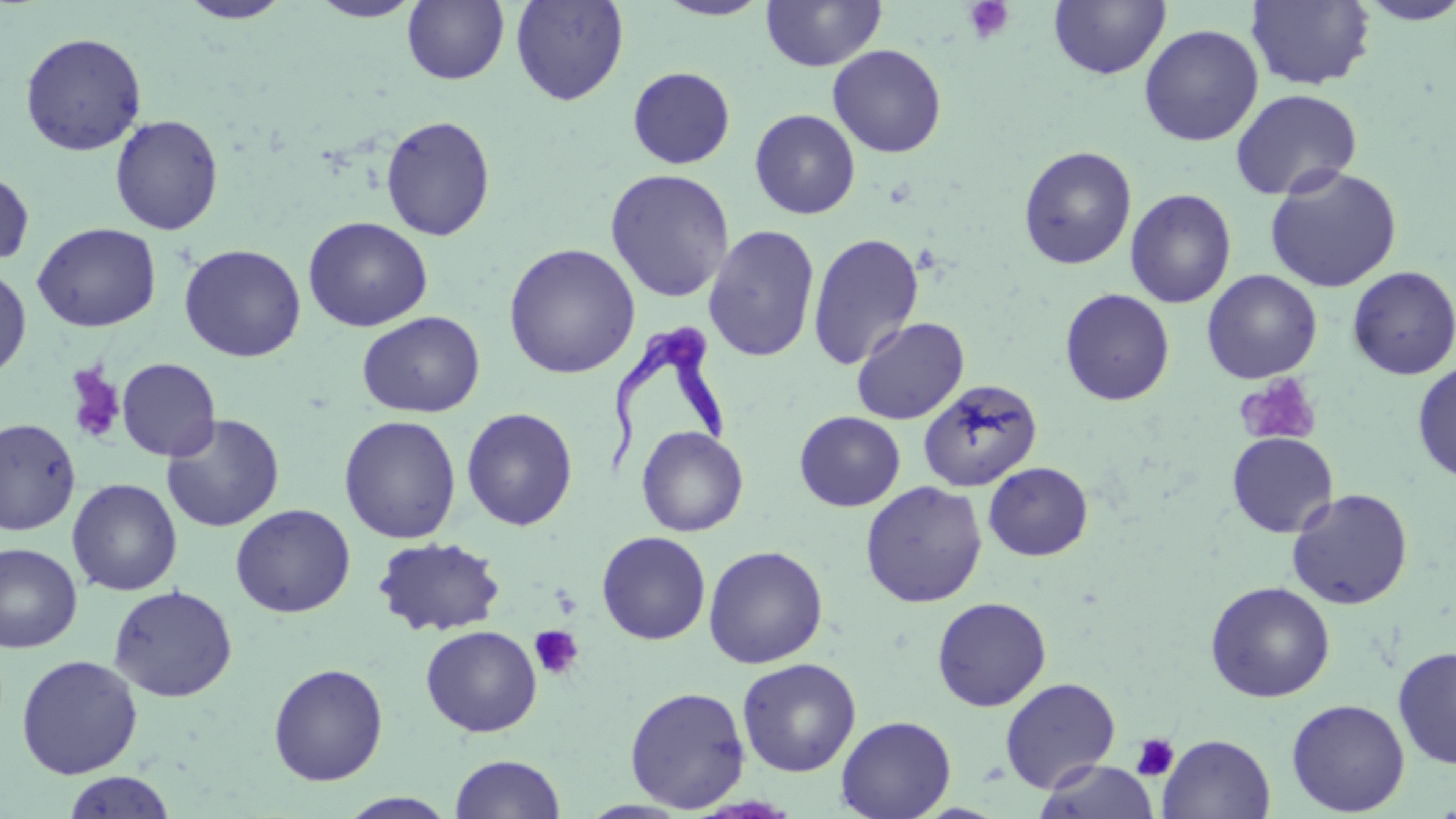
Summary:
  - Coordinate format: approximate bounding boxes as [x1, y1, x2, y2] in pixels
  - Platelet locations: [964, 0, 1015, 43], [64, 363, 125, 444], [1235, 373, 1322, 446], [529, 625, 584, 680], [1131, 733, 1180, 781]
  - Uninfected red blood cell locations: [177, 0, 293, 24], [308, 0, 424, 22], [510, 0, 629, 105], [654, 0, 775, 20], [761, 0, 885, 72], [1353, 0, 1456, 25], [402, 1, 509, 85], [1049, 1, 1171, 80], [1246, 1, 1376, 90], [1139, 24, 1263, 146], [20, 32, 147, 156], [827, 44, 947, 158], [627, 66, 736, 169], [1230, 89, 1362, 201], [749, 109, 861, 219], [109, 114, 224, 236], [380, 115, 496, 241], [1018, 145, 1137, 269], [1264, 166, 1402, 293], [604, 168, 735, 303], [0, 169, 35, 268], [1125, 188, 1236, 308], [303, 216, 433, 332], [32, 222, 161, 333], [703, 225, 820, 362], [808, 232, 924, 370], [503, 243, 640, 379], [179, 244, 306, 362], [0, 265, 32, 380], [1347, 266, 1456, 379], [1202, 270, 1322, 384], [1060, 288, 1175, 406], [357, 311, 485, 418], [851, 316, 969, 424], [116, 357, 221, 462], [1412, 362, 1456, 483], [918, 380, 1042, 491], [461, 407, 578, 531], [794, 411, 905, 511], [161, 413, 285, 532], [339, 415, 462, 544], [1, 418, 81, 536], [637, 426, 749, 537], [1226, 432, 1339, 538], [983, 462, 1093, 561], [67, 478, 182, 596], [860, 480, 987, 607], [1286, 488, 1414, 610], [230, 504, 355, 618], [596, 531, 711, 645], [372, 536, 506, 637], [0, 543, 83, 654], [703, 545, 828, 669], [1204, 581, 1336, 703], [108, 585, 237, 702], [932, 597, 1052, 711], [421, 625, 541, 737], [1393, 644, 1456, 770], [16, 654, 143, 779], [736, 657, 862, 777], [267, 662, 389, 786], [999, 677, 1121, 794], [624, 685, 751, 811], [1286, 699, 1409, 816], [836, 715, 956, 819], [1158, 734, 1275, 819], [449, 754, 566, 818], [1035, 760, 1160, 819], [61, 771, 177, 818], [337, 792, 459, 818]
  - Trypanosoma brucei locations: [602, 315, 733, 475]
  - Slide-level diagnosis: Trypanosoma brucei
  - Stain: May-Grünwald-Giemsa
  - Preparation: thin blood film
  - Image size: 1456×819 pixels
  - Field of view: single
  - Modality: optical microscopy
  - Magnification: 1000x